Draw a bounding box around every leukocyte (white blood cell).
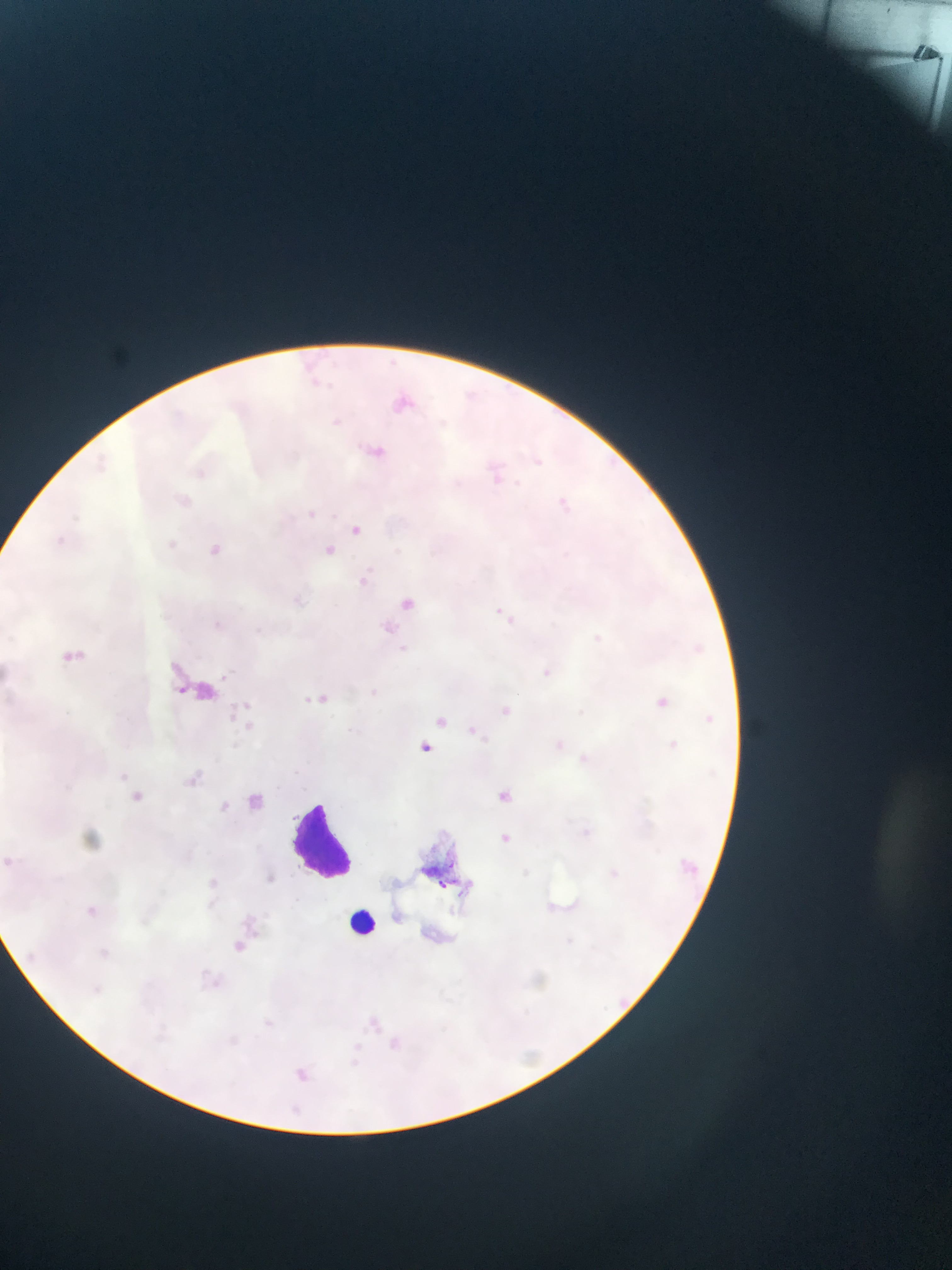

Approximate bounding boxes as {left, top, right, bottom} in pixels.
Leukocytes: {294, 800, 358, 874}, {343, 904, 390, 947}.

Summary:
  - Plasmodium parasite locations: {385, 384, 421, 420}, {356, 439, 393, 468}, {489, 464, 512, 485}, {298, 506, 319, 523}, {349, 518, 368, 542}, {202, 538, 227, 561}, {318, 540, 346, 565}, {350, 570, 386, 600}, {396, 594, 422, 615}, {490, 599, 509, 622}, {57, 640, 92, 677}, {536, 664, 551, 679}, {303, 687, 336, 710}, {219, 695, 256, 725}, {656, 696, 669, 708}, {491, 699, 516, 721}, {425, 706, 444, 729}, {704, 713, 715, 723}, {465, 720, 476, 729}, {420, 739, 441, 756}, {575, 749, 590, 770}, {189, 758, 221, 796}, {250, 783, 289, 808}, {498, 783, 518, 804}, {131, 788, 159, 811}, {215, 795, 234, 821}, {494, 826, 513, 848}, {678, 843, 708, 885}, {0, 849, 18, 867}, {266, 873, 276, 885}, {87, 901, 108, 924}, {216, 931, 255, 958}, {357, 1003, 387, 1038}, {372, 1032, 407, 1055}, {288, 1061, 305, 1078}, {290, 1100, 305, 1117}
  - Image size: 952×1270 pixels
  - Capture: mobile-phone photograph through a microscope
  - Country: Ghana
  - Preparation: thin blood film
  - Field of view: single